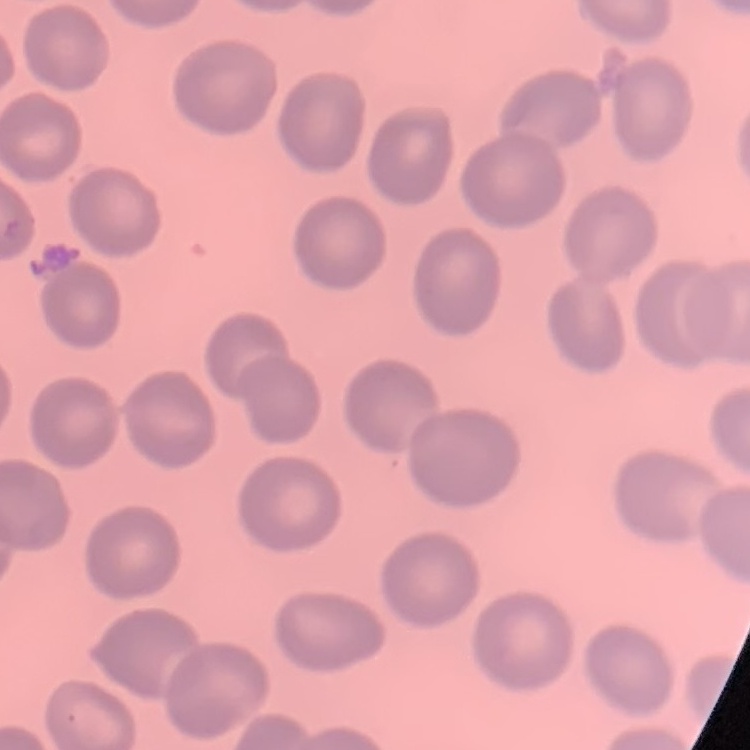

red blood cell morphology = no rouleaux formation
image type = one tile cut from a larger photomicrograph
preparation = thin blood smear
stain = Field's or Giemsa